Locate and identify every blood parasite.
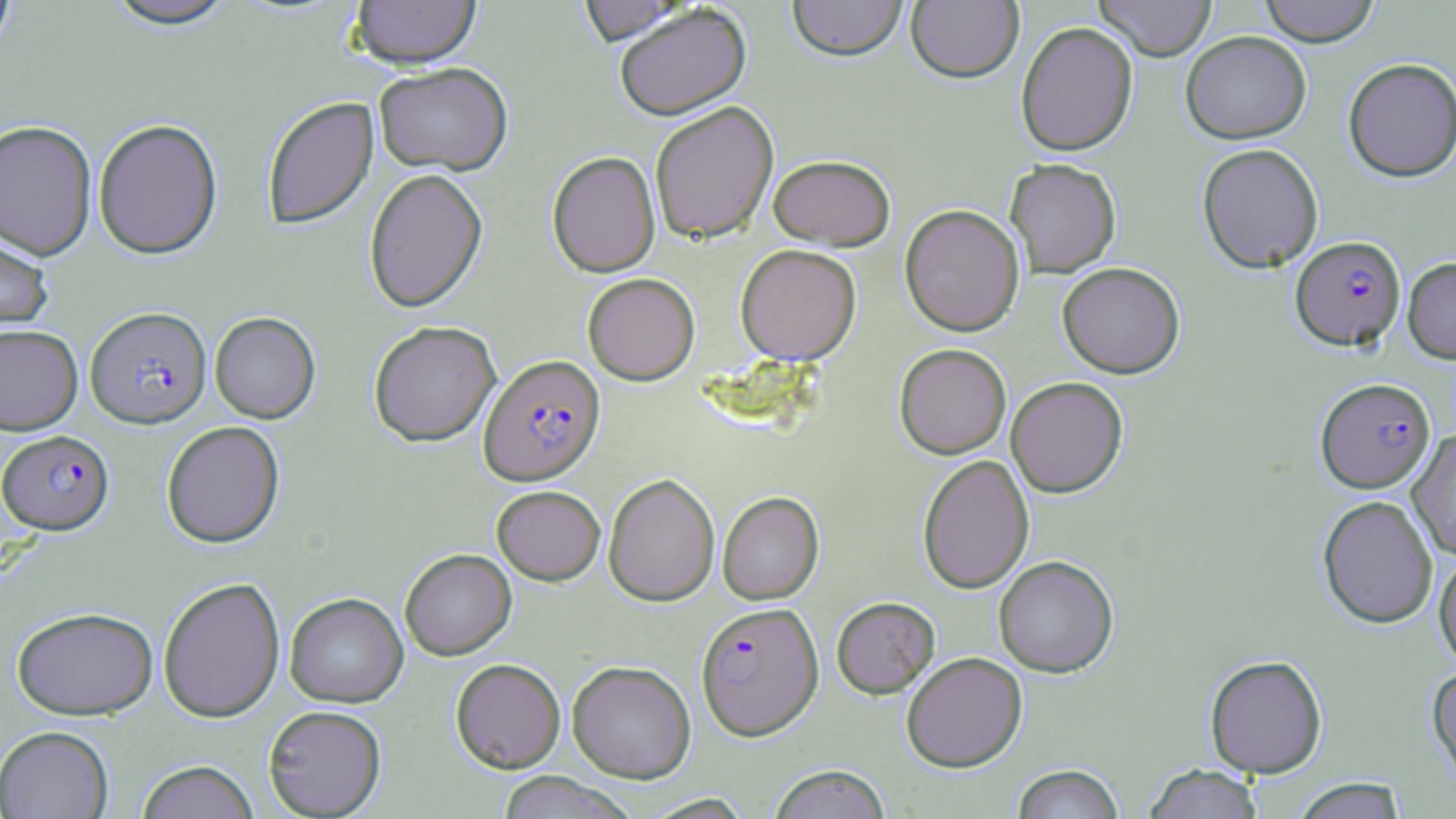

Approximate bounding boxes as (x1, y1, x2, y2) in pixels.
Plasmodium falciparum-infected red blood cells: (1290, 236, 1406, 352), (85, 307, 212, 429), (478, 356, 605, 486), (1316, 379, 1435, 494), (1, 430, 114, 535), (696, 603, 823, 741).
No Plasmodium ovale, Plasmodium malariae, Plasmodium vivax, Babesia divergens, or Trypanosoma brucei observed.

Uninfected red blood cell locations: (0, 0, 17, 57), (102, 0, 237, 32), (350, 0, 482, 73), (576, 0, 694, 48), (787, 0, 907, 65), (1094, 0, 1217, 61), (1259, 0, 1381, 47), (906, 1, 1023, 85), (615, 5, 752, 123), (1016, 22, 1138, 157), (1180, 32, 1311, 144), (1343, 59, 1456, 183), (374, 65, 513, 178), (262, 97, 379, 231), (650, 102, 779, 245), (93, 120, 223, 260), (0, 122, 97, 260), (1197, 143, 1324, 274), (547, 151, 661, 278), (768, 156, 896, 252), (1005, 159, 1121, 278), (364, 169, 487, 313), (899, 204, 1024, 337), (0, 228, 53, 336), (735, 244, 861, 366), (1403, 258, 1456, 364), (1057, 263, 1185, 379), (582, 273, 700, 385), (210, 312, 320, 424), (368, 321, 501, 448), (0, 325, 83, 436), (894, 344, 1011, 459), (1005, 377, 1128, 498), (161, 421, 285, 549), (1406, 429, 1456, 560), (917, 454, 1034, 594), (604, 473, 720, 607), (492, 486, 605, 585), (717, 491, 824, 605), (1317, 495, 1438, 630), (400, 549, 516, 660), (1433, 551, 1456, 671), (993, 556, 1119, 678), (159, 577, 285, 723), (284, 593, 408, 707), (832, 597, 940, 698), (12, 606, 157, 720), (901, 652, 1027, 772), (1204, 655, 1328, 779), (450, 659, 566, 773), (567, 661, 696, 782), (1426, 664, 1456, 793), (263, 705, 387, 818), (0, 725, 114, 818), (135, 760, 259, 819), (767, 764, 892, 819), (1012, 764, 1125, 819), (1142, 764, 1263, 818), (494, 772, 638, 819), (1292, 778, 1407, 819). Slide-level diagnosis: Plasmodium falciparum. One field of a larger specimen. Captured at 1000x magnification. Thin blood smear. Light microscopy. Image is 1456×819 pixels. May-Grünwald-Giemsa-stained preparation.